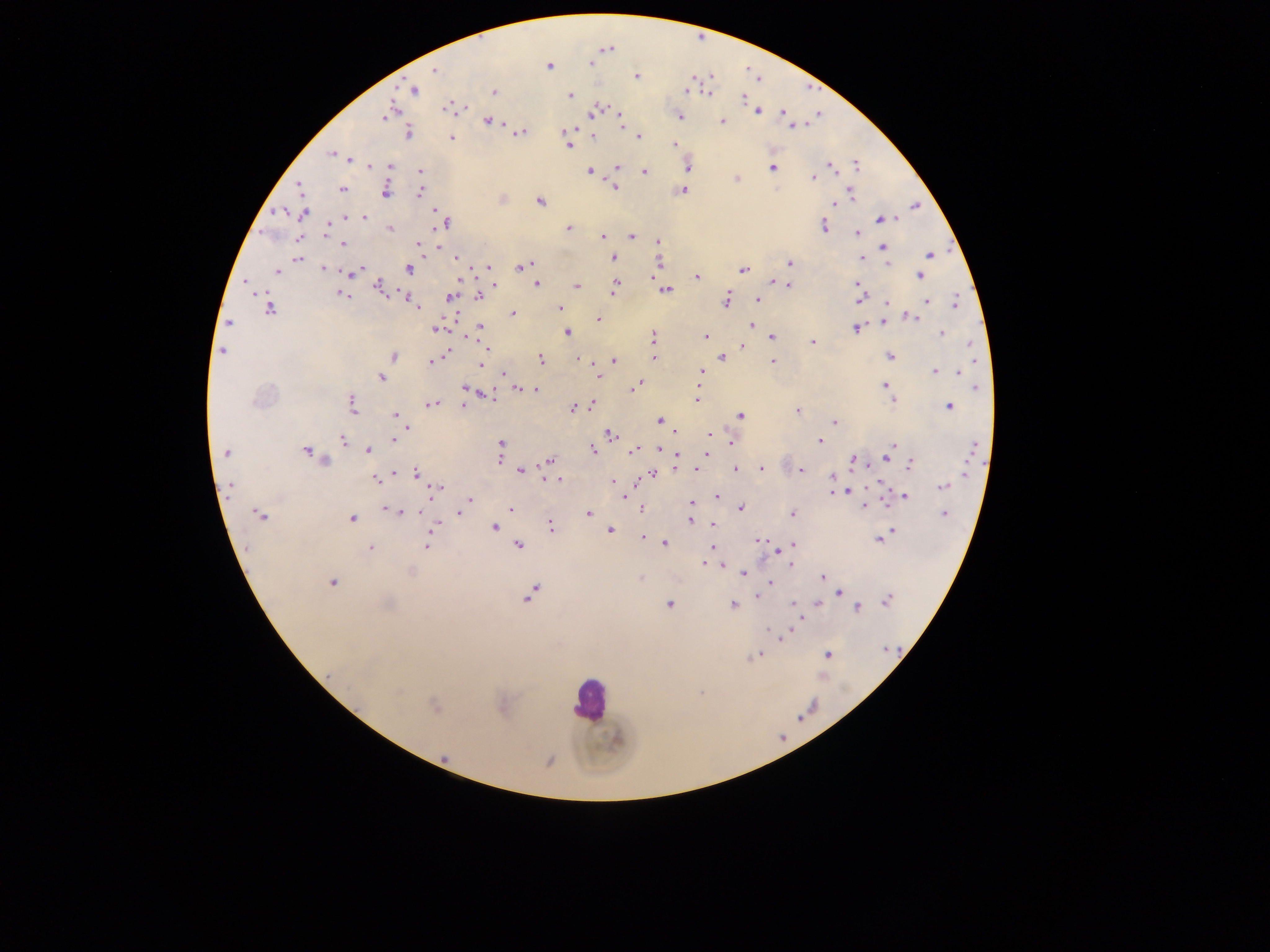
Approximate centers as [x, y] in pixels.
Summary:
  - Malaria parasite locations: [591, 63], [549, 66], [435, 69], [636, 77], [692, 79], [414, 90], [687, 90], [493, 92], [709, 92], [570, 95], [743, 98], [447, 107], [596, 110], [757, 111], [783, 112], [388, 113], [679, 116], [620, 119], [488, 120], [722, 121], [792, 125], [567, 131], [409, 132], [521, 133], [594, 137], [639, 137], [452, 138], [674, 144], [568, 145], [332, 154], [349, 159], [856, 164], [371, 166], [390, 166], [687, 167], [772, 167], [832, 167], [617, 168], [420, 172], [589, 172], [645, 172], [813, 178], [736, 179], [299, 185], [615, 186], [342, 190], [386, 190], [683, 190], [420, 192], [850, 192], [540, 201], [835, 203], [915, 206], [277, 212], [303, 213], [365, 217], [346, 218], [882, 219], [445, 223], [824, 226], [327, 227], [568, 228], [390, 229], [856, 233], [602, 236], [631, 236], [659, 241], [343, 244], [418, 244], [883, 246], [439, 247], [929, 255], [613, 258], [860, 258], [297, 259], [457, 260], [658, 262], [789, 262], [887, 264], [525, 265], [488, 267], [520, 267], [323, 268], [408, 269], [743, 270], [277, 271], [357, 272], [919, 276], [697, 277], [460, 278], [773, 282], [537, 284], [856, 284], [494, 285], [789, 285], [378, 286], [577, 286], [615, 286], [666, 290], [342, 294], [479, 296], [406, 297], [451, 297], [859, 298], [757, 299], [727, 300], [926, 301], [957, 302], [413, 303], [886, 303], [416, 306], [559, 308], [269, 309], [512, 314], [885, 317], [913, 318], [598, 319], [883, 321], [751, 325], [481, 328], [856, 328], [436, 329], [567, 332], [941, 334], [706, 336], [653, 337], [772, 337], [812, 342], [971, 345], [741, 347], [223, 351], [444, 355], [394, 356], [722, 357], [890, 357], [654, 358], [541, 360], [579, 360], [614, 361], [434, 362], [772, 363], [481, 364], [935, 371], [700, 372], [959, 373], [505, 374], [598, 376], [382, 378], [885, 385], [635, 386], [976, 387], [465, 388], [519, 388], [535, 390], [487, 395], [891, 399], [696, 400], [352, 405], [430, 405], [591, 405], [463, 406], [949, 406], [573, 408], [796, 411], [395, 415], [741, 416], [660, 421], [835, 422], [611, 434], [710, 434], [394, 438], [342, 441], [820, 441], [732, 442], [500, 444], [893, 446], [973, 448], [660, 449], [368, 450], [593, 450], [635, 450], [306, 451], [226, 453], [889, 453], [706, 454], [678, 457], [885, 457], [499, 459], [549, 460], [854, 460], [324, 461], [910, 465], [761, 468], [695, 469], [735, 469], [520, 470], [800, 470], [416, 473], [652, 475], [833, 477], [376, 480], [557, 480], [614, 481], [230, 487], [943, 487], [437, 488], [846, 490], [837, 492], [624, 495], [905, 496], [718, 497], [469, 499], [692, 503], [864, 506], [740, 508], [511, 509], [641, 509], [388, 510], [398, 511], [418, 511], [460, 512], [589, 514], [792, 514], [943, 514], [260, 516], [351, 518], [690, 521], [713, 525], [436, 526], [551, 526], [495, 527], [432, 530], [610, 530], [890, 532], [642, 538], [879, 538], [758, 539], [665, 543], [519, 545], [793, 545], [427, 546], [370, 547], [712, 548], [704, 563], [721, 565], [791, 565], [743, 573], [823, 577], [640, 578], [332, 583], [770, 583], [840, 593], [529, 596], [758, 596], [887, 600], [817, 603], [388, 604], [669, 605], [734, 605], [794, 605], [858, 608], [784, 636], [886, 649], [827, 654], [754, 656], [397, 691], [434, 706], [444, 758]
  - Leukocyte locations: [588, 699]
  - Capture: mobile-phone photograph through a microscope
  - Image size: 1270×952 pixels
  - Field of view: single
  - Country: Ghana
  - Preparation: thick blood smear